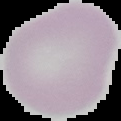

Summary:
  - Preparation: thin blood film
  - Image type: segmented cell region with the area outside set to black
  - Result: no malaria parasites seen
  - Image size: 121×121 pixels